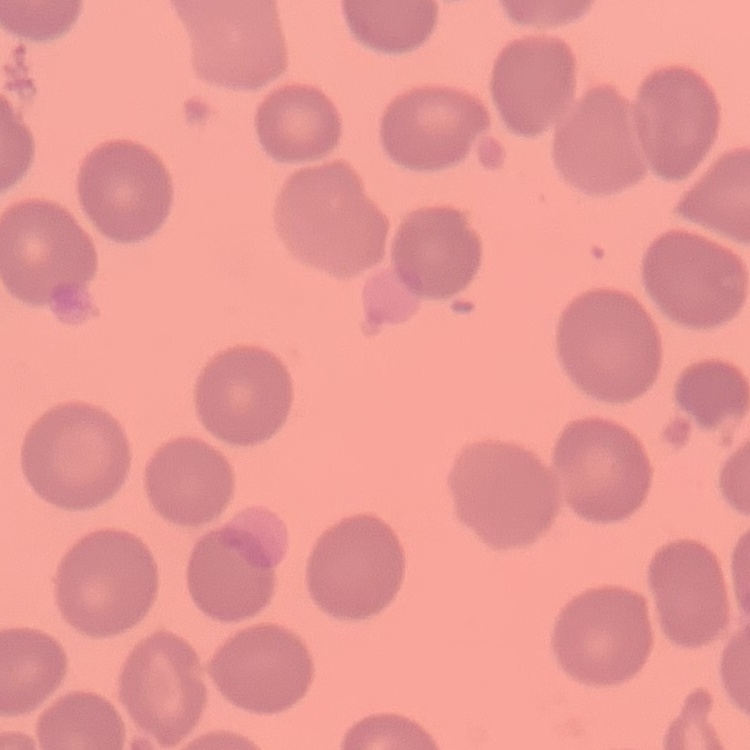
erythrocyte morphology = no rouleaux formation
preparation = thin peripheral smear
image type = one tile cut from a larger photomicrograph
stain = Field's or Giemsa